Name the parasite shown.
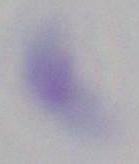

This is Toxoplasma gondii.

magnification = 1000x
modality = micrograph